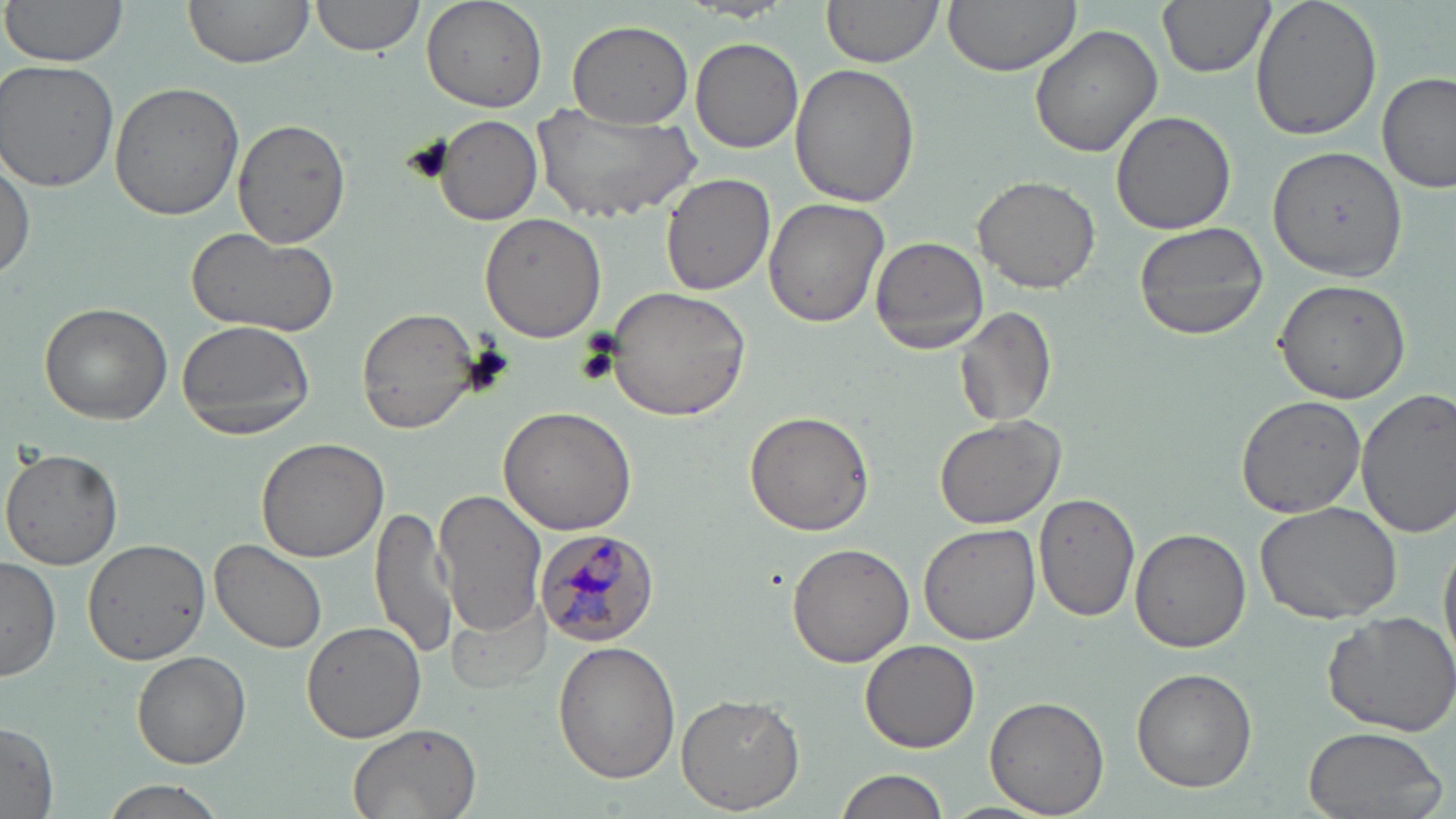
{
  "slide_level_diagnosis": "Plasmodium malariae",
  "modality": "light microscopy",
  "field_of_view": "one of a larger specimen",
  "stain": "May-Grünwald-Giemsa",
  "plasmodium_malariae_infected_red_blood_cell_locations": "approximate bounding boxes as (x1,y1)-(x2,y2) corner pairs in pixels: (534,527)-(662,644)",
  "uninfected_red_blood_cell_locations": "approximate bounding boxes as (x1,y1)-(x2,y2) corner pairs in pixels: (2,0)-(130,71), (183,0)-(313,69), (310,0)-(426,57), (820,0)-(945,70), (938,0)-(1082,75), (1157,0)-(1275,78), (1248,0)-(1385,141), (420,1)-(546,112), (565,19)-(694,128), (1029,24)-(1165,158), (691,36)-(804,154), (0,62)-(121,191), (791,63)-(919,209), (1377,71)-(1453,195), (109,82)-(243,221), (533,105)-(699,224), (1111,109)-(1237,237), (434,113)-(542,226), (231,118)-(353,250), (1268,143)-(1408,285), (0,149)-(34,280), (646,168)-(771,400), (660,174)-(775,294), (972,175)-(1101,294), (763,197)-(892,329), (479,213)-(606,341), (1132,220)-(1270,341), (187,228)-(341,343), (869,235)-(992,354), (1272,279)-(1412,405), (604,285)-(751,422), (39,302)-(173,425), (954,305)-(1057,429), (356,308)-(481,433), (174,318)-(317,440), (1356,388)-(1456,537), (1235,394)-(1366,518), (498,405)-(638,536), (743,411)-(874,536), (933,413)-(1064,529), (255,437)-(390,563), (1,447)-(124,571), (434,490)-(548,636), (1035,493)-(1139,621), (1254,500)-(1403,622), (369,502)-(459,660), (917,522)-(1041,646), (1130,528)-(1251,652), (83,538)-(213,667), (210,539)-(327,654), (785,540)-(914,667), (0,557)-(61,682), (446,594)-(550,696), (1322,609)-(1456,736), (302,620)-(427,742), (860,639)-(981,752), (552,640)-(679,783), (131,651)-(250,768), (1131,667)-(1257,791), (675,693)-(803,815), (983,695)-(1109,815), (0,720)-(59,814), (343,721)-(483,819), (1300,725)-(1448,819), (836,768)-(948,819), (97,778)-(233,819), (940,800)-(1055,819)",
  "magnification": "1000x",
  "image_size": "1456×819 pixels",
  "preparation": "thin blood film"
}